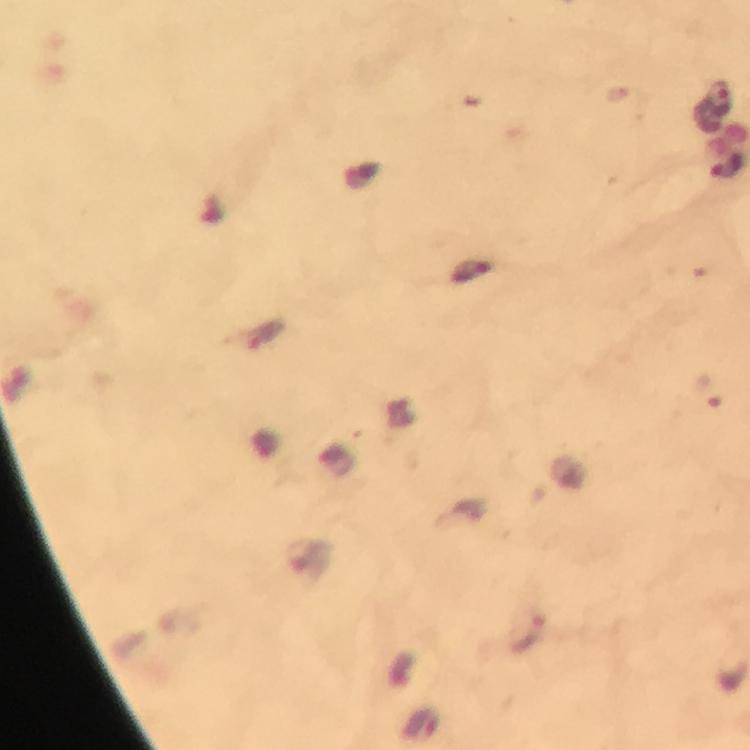
cropped_from: one field of view
image_size: 750×750 pixels
malaria_parasite_locations: 'approximate centers as (x, y) in pixels: (720, 96), (728, 165), (527, 633)'
capture: smartphone photograph through a microscope
immersion_oil: used
preparation: thick blood film
magnification: 100x
stain: Giemsa
context: from a malaria diagnostic workup